Classify this cell by malaria status.
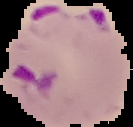

Parasitized.

Summary:
  - Preparation: thin blood film
  - Image type: cell region segmented out of the field of view; surrounding area masked to black
  - Image size: 133×127 pixels